Describe the morphology of the erythrocytes.
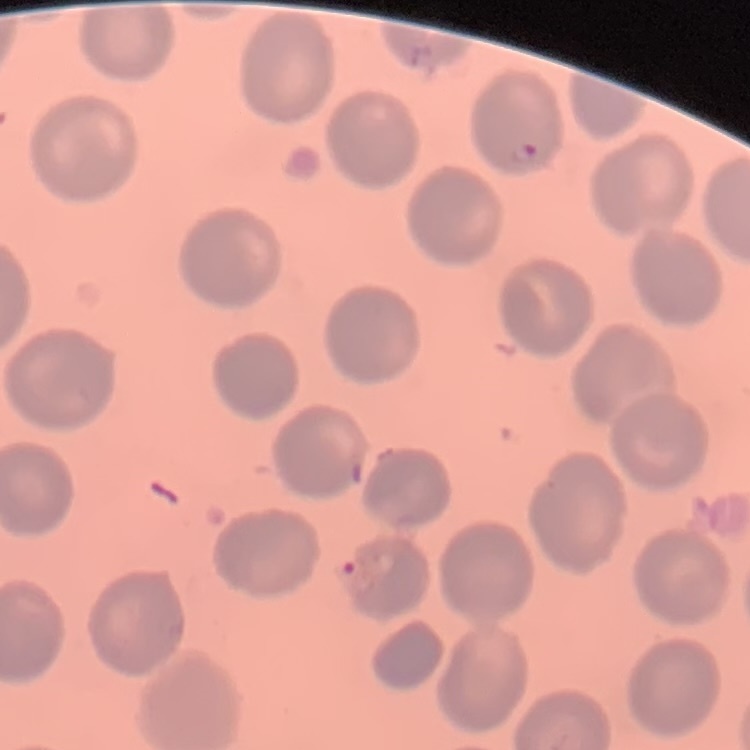

No rouleaux formation.

Field's or Giemsa stain. Square crop of a larger photomicrograph. Thin blood film.